Assess this cell for malaria.
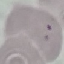

Uninfected.

Summary:
  - Capture: smartphone camera at the microscope eyepiece
  - Stain: Giemsa
  - Preparation: thin smear
  - Image type: automatically extracted cell patch, resized to 64 × 64 pixels